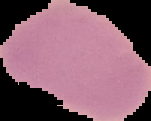

From a thin blood film. Segmented cell region on a black background. Result: no malaria parasites seen. Image is 151×121 pixels.